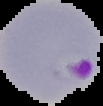 Image is 103×106 pixels. Cell region segmented out of the field of view; the surrounding area is masked to black. Malaria status: parasitized. From a thin blood smear.